State the blood parasite species.
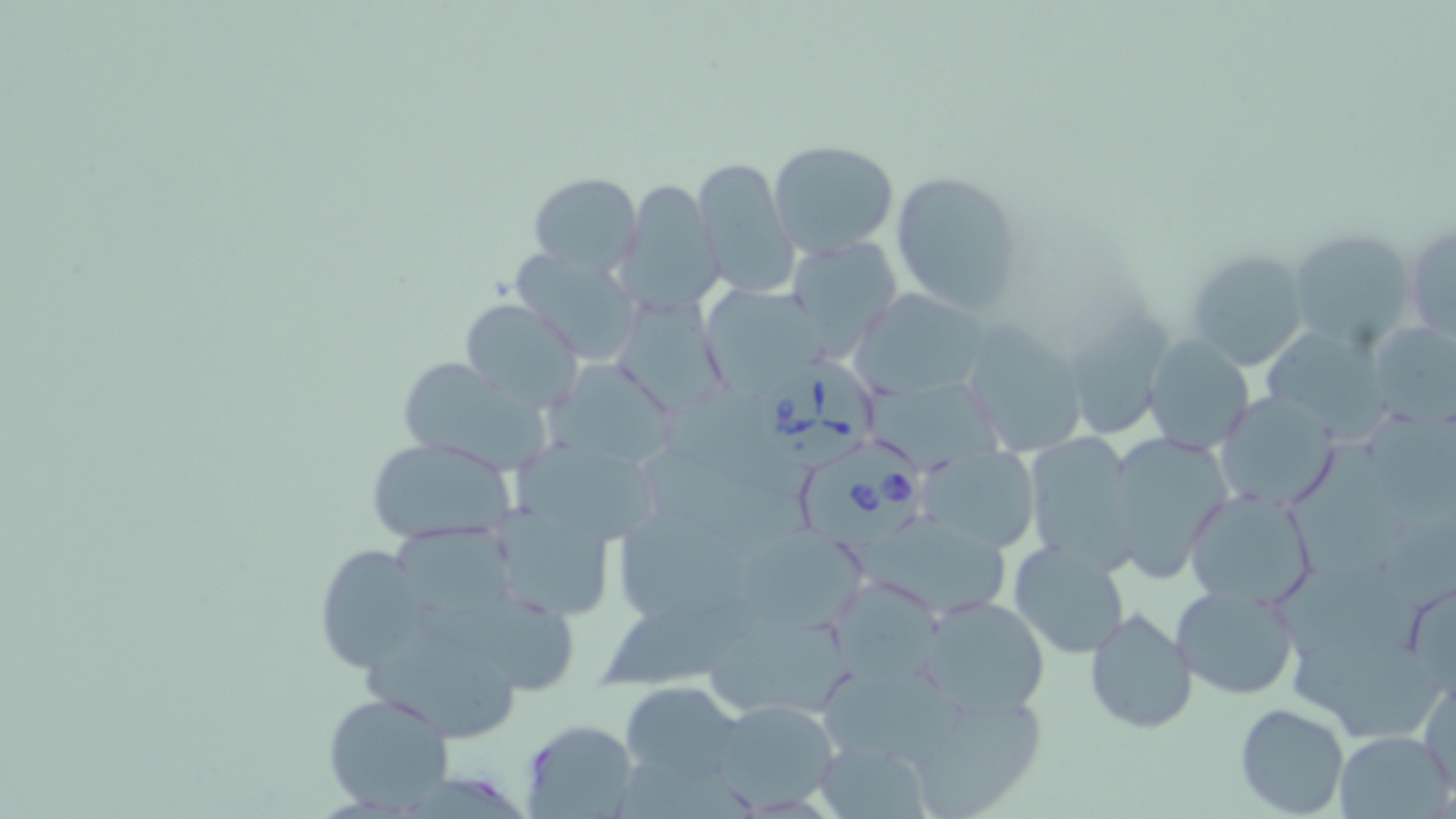

Babesia divergens.

Summary:
  - Coordinate format: approximate bounding boxes as [x1, y1, x2, y2] in pixels
  - Babesia divergens-infected red blood cell locations: [755, 355, 877, 469], [799, 435, 926, 548]
  - Uninfected red blood cell locations: [768, 140, 898, 258], [692, 157, 798, 301], [890, 170, 1027, 314], [528, 172, 643, 275], [615, 179, 723, 315], [1404, 219, 1455, 343], [1288, 230, 1421, 350], [786, 238, 902, 357], [1185, 248, 1311, 371], [508, 249, 644, 367], [702, 288, 831, 394], [607, 293, 731, 417], [853, 293, 995, 402], [460, 299, 583, 413], [1074, 308, 1179, 447], [1370, 320, 1456, 428], [962, 325, 1091, 458], [1262, 330, 1389, 449], [1141, 336, 1255, 455], [395, 357, 548, 474], [552, 360, 674, 468], [662, 389, 811, 501], [1214, 392, 1343, 511], [1102, 431, 1234, 581], [1022, 433, 1138, 570], [367, 436, 519, 547], [1286, 445, 1419, 581], [923, 446, 1037, 556], [513, 447, 663, 544], [1182, 488, 1317, 610], [487, 495, 622, 623], [621, 508, 780, 624], [398, 526, 532, 617], [749, 534, 879, 635], [1009, 538, 1131, 660], [310, 543, 428, 673], [1278, 559, 1441, 674], [607, 582, 765, 688], [1170, 582, 1301, 702], [831, 584, 948, 688], [917, 595, 1053, 717], [420, 596, 582, 689], [1084, 607, 1198, 734], [708, 621, 859, 715], [1293, 626, 1447, 742], [362, 647, 517, 737], [1420, 677, 1456, 793], [619, 680, 748, 786], [904, 689, 1045, 818], [322, 691, 456, 813], [708, 697, 841, 812], [1234, 704, 1351, 817], [519, 719, 640, 819], [1334, 730, 1454, 818], [814, 736, 935, 818]
  - Stain: May-Grünwald-Giemsa
  - Field of view: one of a larger specimen
  - Image size: 1456×819 pixels
  - Magnification: 1000x
  - Modality: optical microscopy
  - Preparation: thin blood film